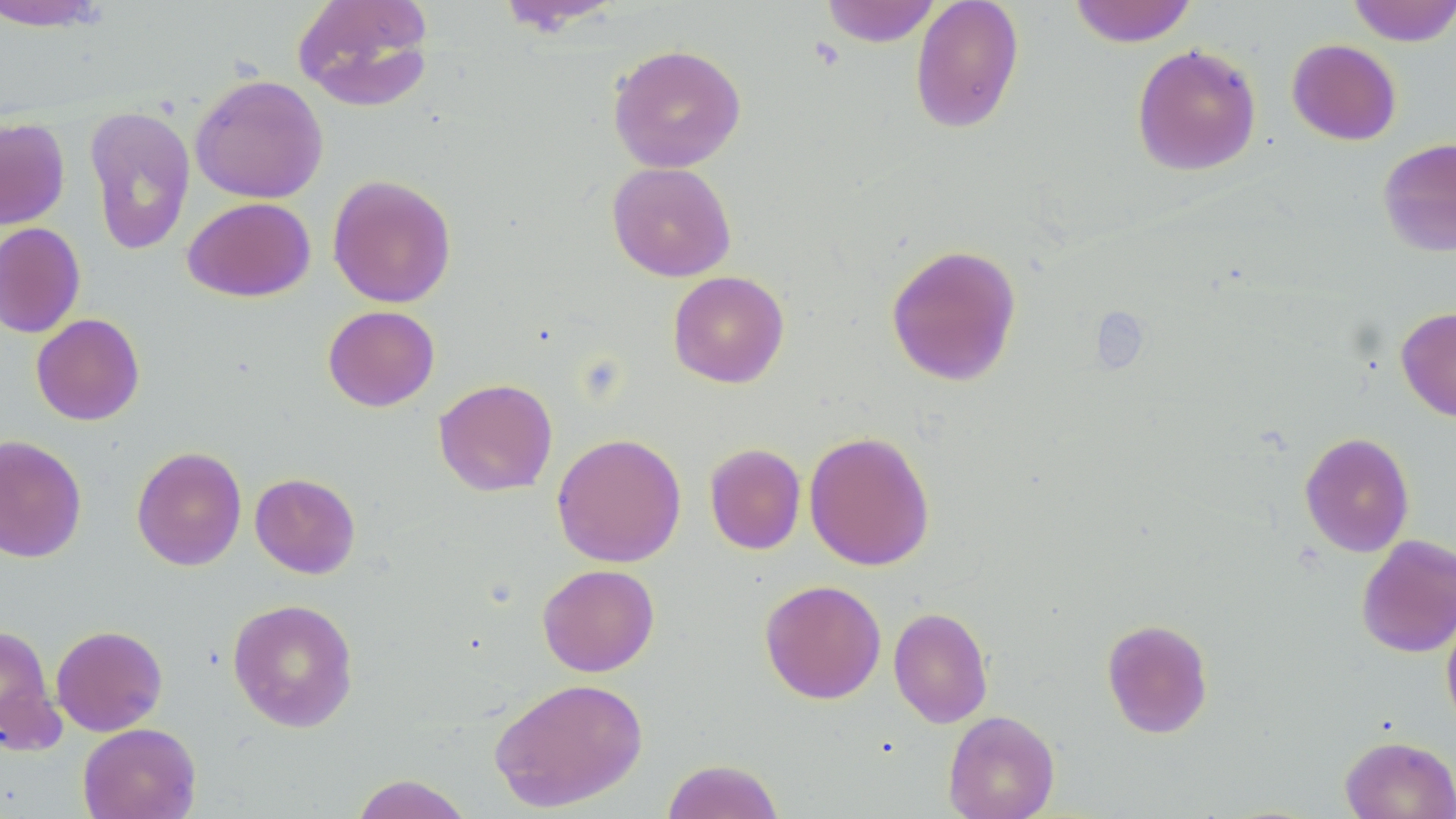
Approximate bounding boxes as [x1, y1, x2, y2] in pixels. Uninfected red blood cell locations: [292, 0, 436, 112], [820, 0, 942, 47], [910, 0, 1024, 134], [1068, 0, 1198, 47], [0, 1, 112, 31], [493, 1, 627, 34], [1346, 1, 1456, 46], [1286, 38, 1401, 145], [608, 43, 747, 173], [1131, 44, 1262, 176], [190, 73, 329, 204], [84, 105, 196, 256], [0, 117, 71, 229], [1378, 137, 1456, 257], [606, 161, 736, 282], [327, 174, 457, 308], [182, 197, 316, 302], [0, 222, 85, 338], [885, 243, 1022, 386], [667, 270, 789, 388], [323, 305, 440, 412], [1396, 307, 1456, 422], [31, 313, 145, 425], [433, 378, 558, 497], [804, 431, 935, 571], [1299, 431, 1415, 557], [551, 432, 686, 567], [0, 435, 87, 563], [704, 443, 806, 555], [131, 446, 247, 571], [250, 472, 361, 579], [1356, 534, 1456, 659], [537, 563, 659, 677], [759, 579, 887, 705], [227, 598, 359, 733], [888, 606, 994, 728], [1441, 608, 1456, 733], [1101, 618, 1214, 738], [0, 624, 63, 754], [51, 624, 168, 736], [489, 676, 648, 811], [942, 710, 1060, 819], [78, 723, 201, 819], [1340, 735, 1456, 819], [661, 758, 785, 819], [349, 774, 475, 819]. Slide-level diagnosis: negative for blood parasites. 1000x magnification. Thin blood film. May-Grünwald-Giemsa stain. Image is 1456×819 pixels. Light microscopy. One field of a larger specimen.